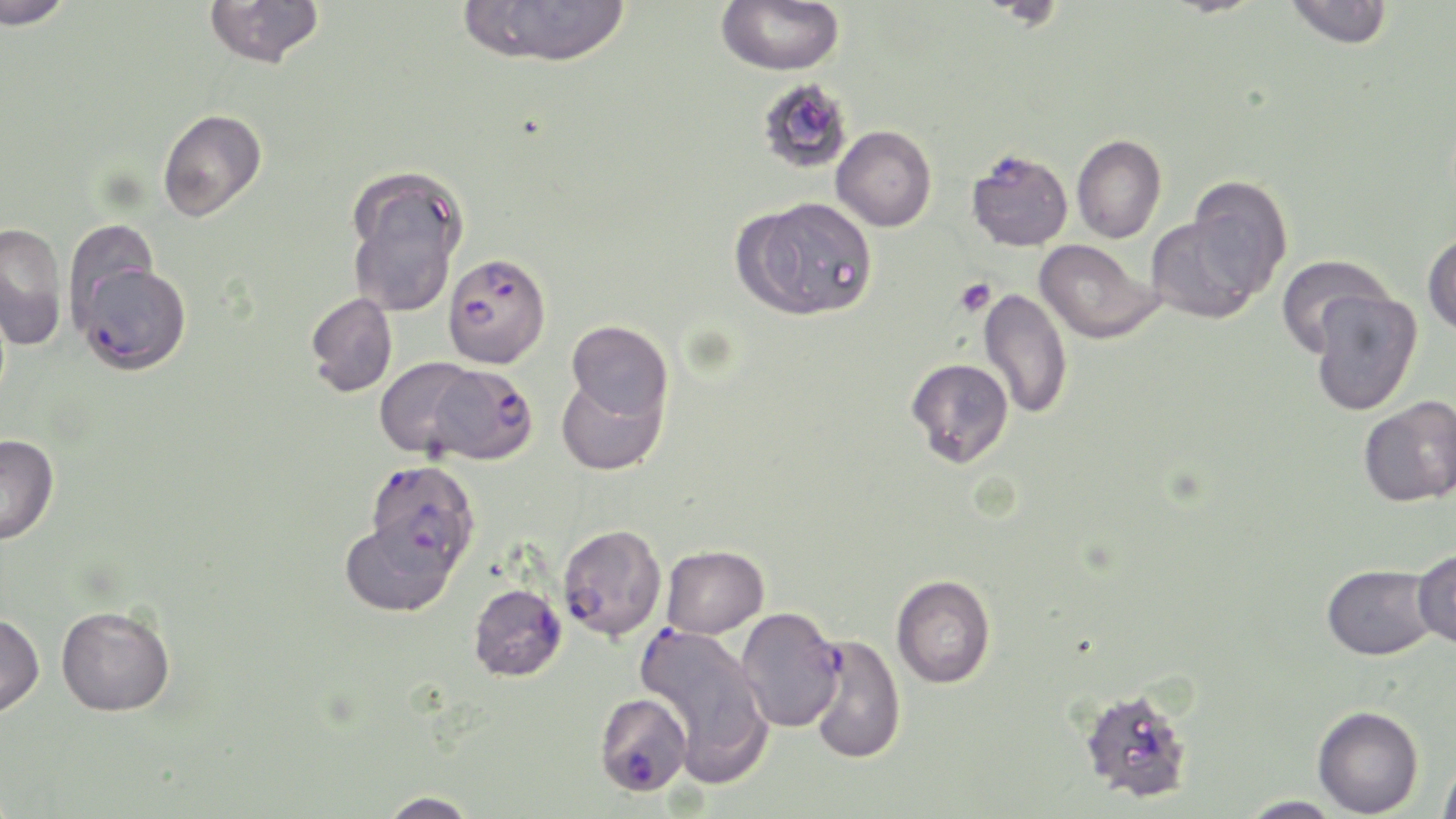
{
  "slide_level_diagnosis": "Plasmodium falciparum",
  "uninfected_red_blood_cell_locations": "approximate bounding boxes as (x1,y1)-(x2,y2) corner pairs in pixels: (0,0)-(73,30), (204,0)-(325,69), (459,0)-(633,67), (716,0)-(844,75), (1283,0)-(1394,49), (765,83)-(848,170), (157,109)-(267,223), (832,125)-(937,231), (1072,134)-(1167,243), (966,149)-(1073,251), (344,167)-(468,317), (1185,176)-(1293,298), (738,197)-(876,320), (1145,214)-(1266,324), (69,218)-(156,335), (0,221)-(69,351), (1423,231)-(1456,337), (1034,239)-(1162,344), (1276,255)-(1394,356), (978,288)-(1072,420), (1308,290)-(1423,416), (305,292)-(398,397), (566,320)-(673,421), (374,357)-(482,458), (906,358)-(1014,468), (556,374)-(668,476), (1359,396)-(1456,507), (0,434)-(59,545), (340,517)-(459,617), (661,545)-(769,639), (1413,548)-(1456,650), (1322,563)-(1438,660), (891,574)-(996,689), (56,604)-(175,717), (735,607)-(844,733), (0,613)-(45,718), (1078,686)-(1196,804), (685,702)-(776,787), (1313,705)-(1424,817), (1438,756)-(1456,817), (376,790)-(483,818), (1236,795)-(1345,818)",
  "stain": "May-Grünwald-Giemsa",
  "field_of_view": "one of a larger specimen",
  "preparation": "thin blood film",
  "platelet_locations": "approximate bounding boxes as (x1,y1)-(x2,y2) corner pairs in pixels: (954,278)-(996,318)",
  "image_size": "1456×819 pixels",
  "magnification": "1000x",
  "plasmodium_falciparum_infected_red_blood_cell_locations": "approximate bounding boxes as (x1,y1)-(x2,y2) corner pairs in pixels: (443,252)-(550,368), (74,261)-(192,374), (425,363)-(538,465), (364,460)-(480,572), (557,523)-(666,642), (468,583)-(567,682), (635,624)-(749,713), (806,634)-(906,763), (594,692)-(693,797)",
  "modality": "light microscopy"
}